Give the position of every Plasmodium parasite visible.
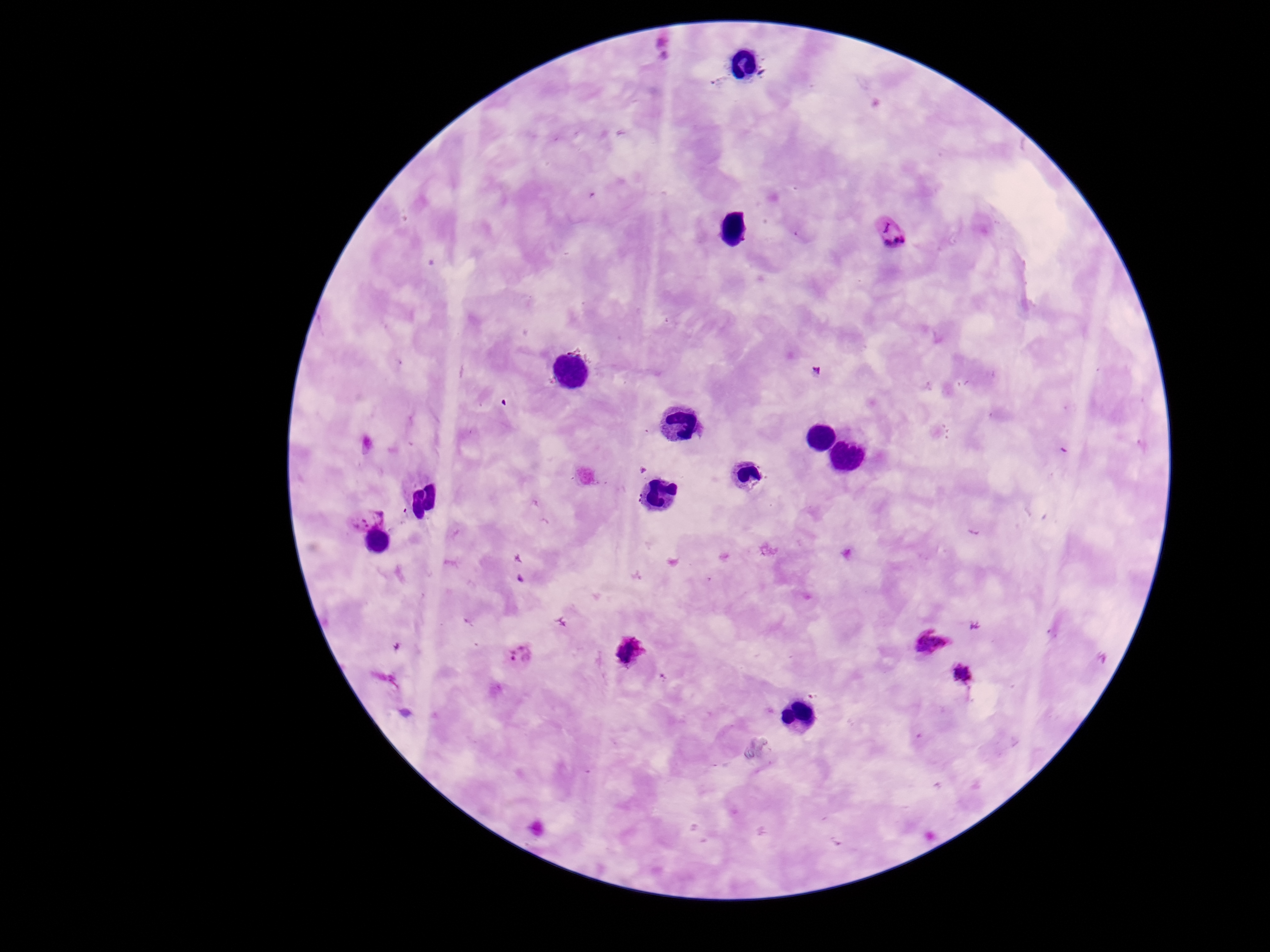
Approximate centers as [x, y] in pixels.
Plasmodium parasites: [891, 234], [363, 516], [928, 644], [631, 653], [518, 656], [963, 674].

Summary:
  - Patient malaria status: infected
  - Field of view: one from this slide
  - Preparation: thick peripheral-blood smear
  - Capture: smartphone camera through the microscope eyepiece
  - Magnification: 100x
  - Image size: 1270×952 pixels
  - Stain: Giemsa